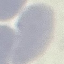
Malaria status: uninfected. Thin smear of blood. Acquired by smartphone through the microscope eyepiece. Automatically extracted cell patch, resized to 64 × 64 pixels. Giemsa stain.